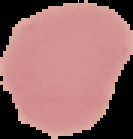
Summary:
  - Image size: 133×139 pixels
  - Preparation: thin blood smear
  - Result: no malaria parasites seen
  - Image type: segmented cell region with the area outside set to black